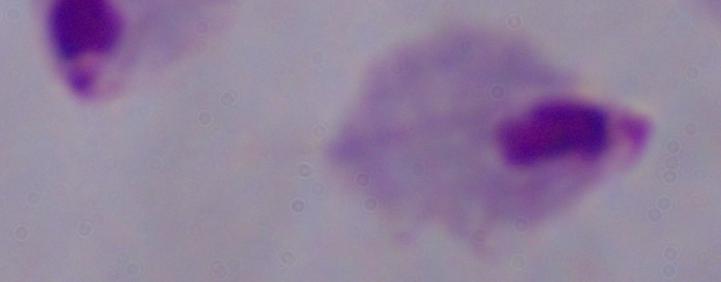 Captured at 1000x magnification. Micrograph. A trichomonad is shown.